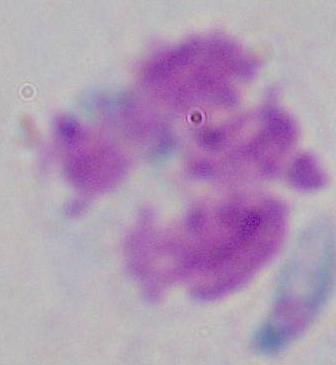
modality: micrograph
identification: white blood cell
magnification: 1000x